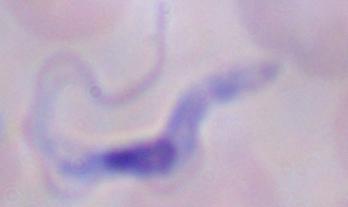
Summary:
  - Magnification: 1000x
  - Modality: micrograph
  - Identification: trypanosome